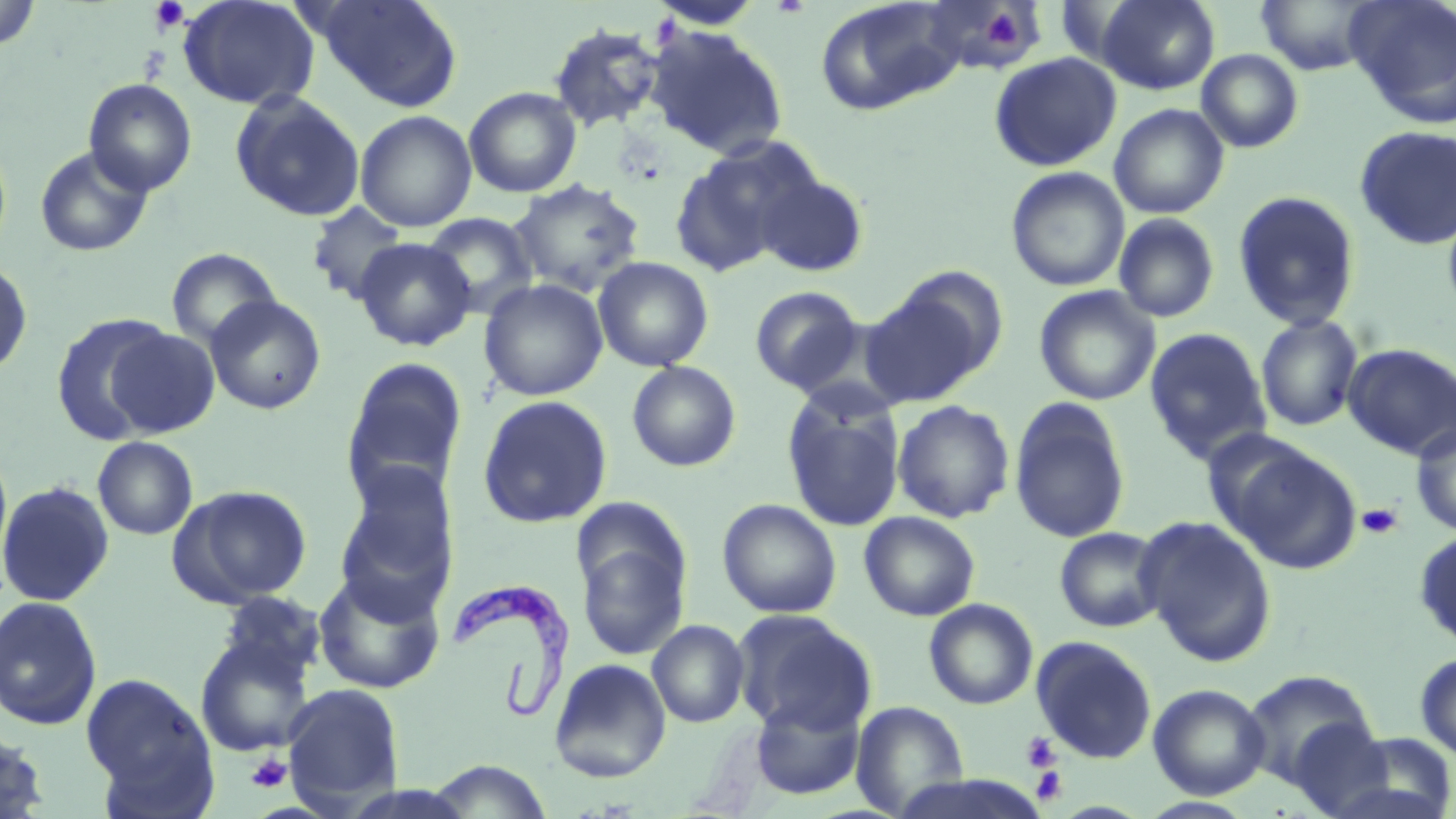
Approximate bounding boxes as [x1, y1, x2, y2] in pixels. Trypanosoma brucei locations: [451, 579, 575, 716]. Platelet locations: [148, 0, 190, 35], [982, 8, 1024, 48], [1357, 503, 1403, 539], [1021, 733, 1061, 772], [247, 753, 292, 793], [1030, 766, 1068, 805]. Uninfected red blood cell locations: [0, 0, 41, 52], [178, 0, 320, 110], [310, 0, 464, 111], [814, 0, 963, 116], [1095, 0, 1219, 94], [1255, 0, 1382, 75], [1343, 0, 1456, 124], [647, 2, 767, 31], [922, 2, 1048, 75], [547, 22, 665, 133], [647, 26, 789, 159], [1196, 49, 1304, 153], [989, 52, 1122, 172], [83, 78, 197, 196], [464, 86, 581, 197], [230, 91, 365, 221], [1108, 103, 1229, 219], [355, 110, 477, 231], [1354, 125, 1456, 249], [669, 142, 807, 278], [34, 144, 154, 258], [1006, 166, 1130, 292], [755, 171, 869, 277], [509, 178, 646, 298], [1232, 190, 1362, 331], [1442, 199, 1456, 321], [307, 202, 411, 306], [422, 212, 539, 318], [1113, 213, 1220, 323], [354, 237, 476, 351], [166, 247, 282, 351], [593, 256, 714, 372], [0, 259, 33, 378], [478, 279, 608, 401], [861, 284, 994, 406], [749, 286, 864, 394], [1034, 286, 1160, 406], [205, 295, 326, 415], [50, 312, 176, 444], [1256, 314, 1363, 432], [103, 327, 220, 437], [1143, 327, 1272, 464], [1342, 343, 1456, 460], [340, 357, 470, 503], [627, 361, 741, 472], [782, 393, 905, 533], [476, 395, 613, 528], [1009, 399, 1131, 544], [892, 400, 1015, 523], [1411, 423, 1456, 537], [93, 436, 198, 540], [1223, 441, 1363, 575], [335, 464, 460, 607], [0, 480, 115, 607], [169, 484, 313, 607], [717, 498, 842, 618], [858, 511, 980, 621], [1136, 516, 1278, 666], [1054, 526, 1167, 632], [1413, 529, 1456, 651], [576, 533, 690, 662], [313, 569, 446, 694], [215, 591, 326, 686], [0, 595, 102, 730], [924, 598, 1038, 710], [733, 610, 875, 735], [647, 619, 750, 728], [195, 633, 316, 757], [1030, 634, 1157, 763], [1414, 652, 1456, 762], [549, 658, 671, 782], [1241, 670, 1377, 786], [80, 672, 215, 804], [282, 682, 405, 812], [1148, 683, 1270, 799], [749, 697, 865, 800], [851, 700, 969, 817], [1286, 720, 1396, 816], [0, 729, 52, 819], [1334, 731, 1456, 819], [427, 760, 553, 819], [1137, 796, 1258, 818]. Slide-level diagnosis: Trypanosoma brucei. Thin blood film. One field of a larger specimen. 1000x magnification. Image is 1456×819 pixels. May-Grünwald-Giemsa stain. Optical microscopy.